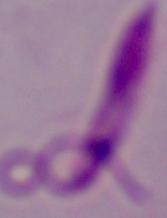
magnification = 1000x
identification = Leishmania
modality = micrograph